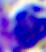
Micrograph. A white blood cell is seen. 400x magnification.